Outline each Plasmodium vivax-infected red blood cell.
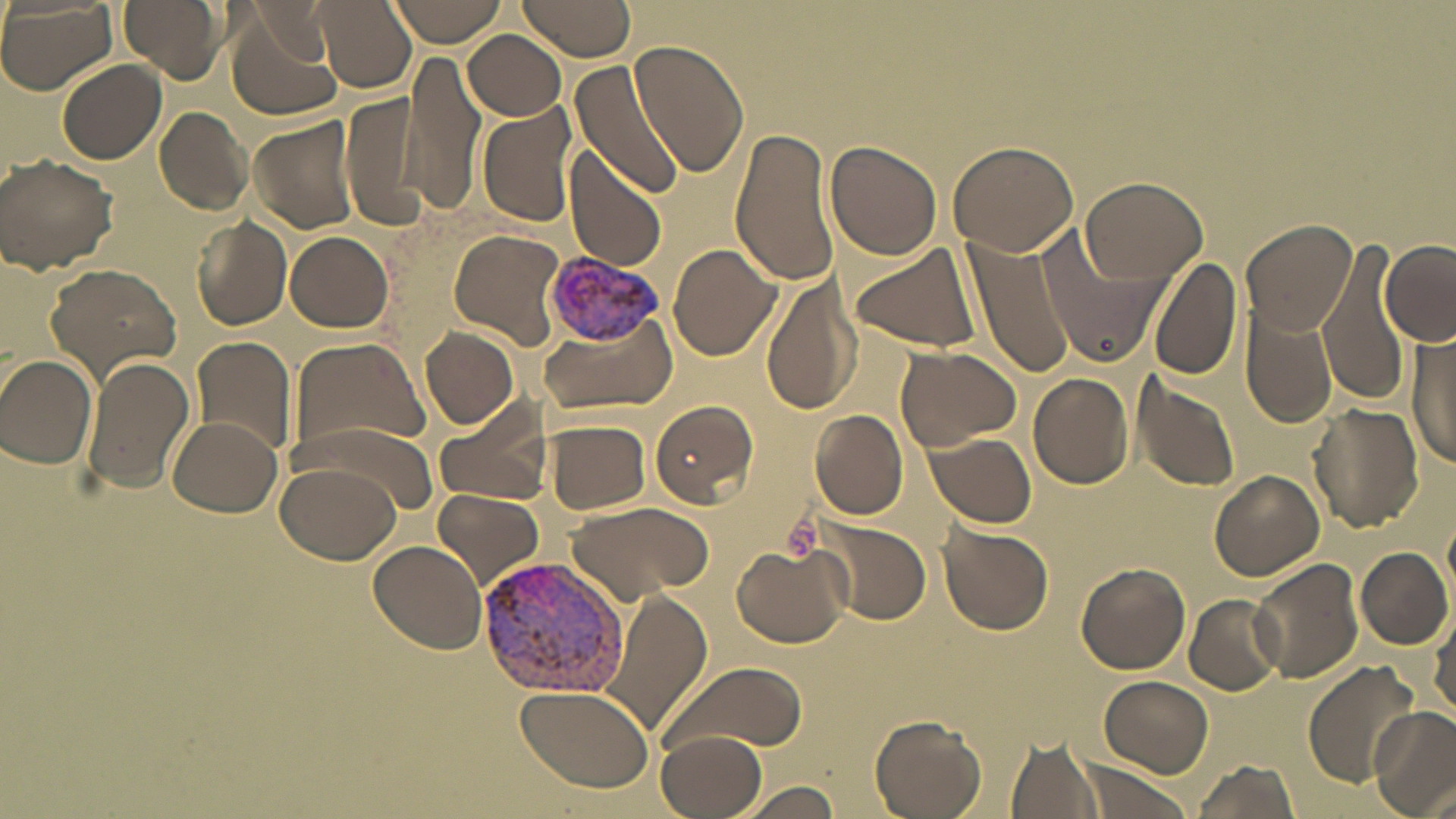
Approximate bounding boxes as named x1/y1/x2/y2 corners in pixels.
Plasmodium vivax-infected red blood cells: (x1=545, y1=248, x2=666, y2=346), (x1=474, y1=550, x2=632, y2=698).

Summary:
  - Platelet locations: (x1=777, y1=496, x2=822, y2=556)
  - Uninfected red blood cell locations: (x1=121, y1=0, x2=226, y2=81), (x1=316, y1=0, x2=417, y2=95), (x1=390, y1=0, x2=509, y2=46), (x1=516, y1=0, x2=637, y2=60), (x1=0, y1=3, x2=117, y2=95), (x1=226, y1=9, x2=345, y2=123), (x1=464, y1=30, x2=567, y2=121), (x1=628, y1=38, x2=747, y2=178), (x1=401, y1=51, x2=488, y2=215), (x1=571, y1=57, x2=688, y2=200), (x1=57, y1=59, x2=167, y2=164), (x1=341, y1=90, x2=428, y2=231), (x1=480, y1=103, x2=577, y2=225), (x1=155, y1=107, x2=254, y2=215), (x1=247, y1=117, x2=361, y2=233), (x1=728, y1=126, x2=840, y2=288), (x1=824, y1=140, x2=942, y2=260), (x1=948, y1=140, x2=1080, y2=257), (x1=563, y1=144, x2=668, y2=273), (x1=1, y1=154, x2=120, y2=276), (x1=1078, y1=176, x2=1207, y2=288), (x1=192, y1=215, x2=292, y2=331), (x1=1242, y1=219, x2=1357, y2=333), (x1=1036, y1=227, x2=1171, y2=369), (x1=967, y1=229, x2=1076, y2=380), (x1=284, y1=230, x2=395, y2=333), (x1=450, y1=230, x2=566, y2=349), (x1=1379, y1=239, x2=1455, y2=348), (x1=846, y1=242, x2=981, y2=357), (x1=669, y1=243, x2=781, y2=360), (x1=1318, y1=244, x2=1411, y2=407), (x1=1149, y1=257, x2=1241, y2=382), (x1=46, y1=262, x2=182, y2=382), (x1=762, y1=271, x2=861, y2=418), (x1=1240, y1=304, x2=1338, y2=429), (x1=539, y1=321, x2=671, y2=417), (x1=421, y1=326, x2=519, y2=430), (x1=1410, y1=326, x2=1455, y2=476), (x1=191, y1=335, x2=297, y2=459), (x1=290, y1=336, x2=431, y2=457), (x1=895, y1=344, x2=1020, y2=450), (x1=1, y1=353, x2=98, y2=469), (x1=81, y1=356, x2=192, y2=492), (x1=1133, y1=372, x2=1241, y2=493), (x1=1027, y1=373, x2=1134, y2=491), (x1=648, y1=399, x2=757, y2=509), (x1=436, y1=402, x2=552, y2=510), (x1=1308, y1=403, x2=1422, y2=533), (x1=810, y1=408, x2=909, y2=519), (x1=166, y1=416, x2=281, y2=518), (x1=294, y1=419, x2=441, y2=517), (x1=544, y1=419, x2=652, y2=514), (x1=552, y1=422, x2=666, y2=602), (x1=924, y1=431, x2=1038, y2=527), (x1=277, y1=461, x2=401, y2=564), (x1=1210, y1=469, x2=1325, y2=580), (x1=431, y1=487, x2=545, y2=594), (x1=566, y1=500, x2=711, y2=606), (x1=1445, y1=515, x2=1456, y2=602), (x1=807, y1=516, x2=933, y2=626), (x1=936, y1=520, x2=1054, y2=636), (x1=370, y1=540, x2=488, y2=653), (x1=733, y1=542, x2=851, y2=648), (x1=1355, y1=546, x2=1452, y2=650), (x1=1248, y1=556, x2=1363, y2=686), (x1=1076, y1=561, x2=1190, y2=675), (x1=596, y1=587, x2=715, y2=734), (x1=1186, y1=595, x2=1284, y2=694), (x1=1431, y1=613, x2=1456, y2=721), (x1=1303, y1=660, x2=1421, y2=787), (x1=660, y1=661, x2=807, y2=761), (x1=1099, y1=675, x2=1212, y2=777), (x1=512, y1=684, x2=657, y2=794), (x1=1369, y1=709, x2=1456, y2=817), (x1=869, y1=712, x2=988, y2=819), (x1=658, y1=731, x2=767, y2=817), (x1=1005, y1=731, x2=1104, y2=818), (x1=1193, y1=758, x2=1303, y2=819), (x1=1080, y1=761, x2=1197, y2=817), (x1=730, y1=780, x2=846, y2=819)
  - Slide-level diagnosis: Plasmodium vivax
  - Magnification: 1000x
  - Field of view: single
  - Preparation: thin blood smear
  - Stain: May-Grünwald-Giemsa
  - Image size: 1456×819 pixels
  - Modality: optical microscopy